Point out each Plasmodium parasite.
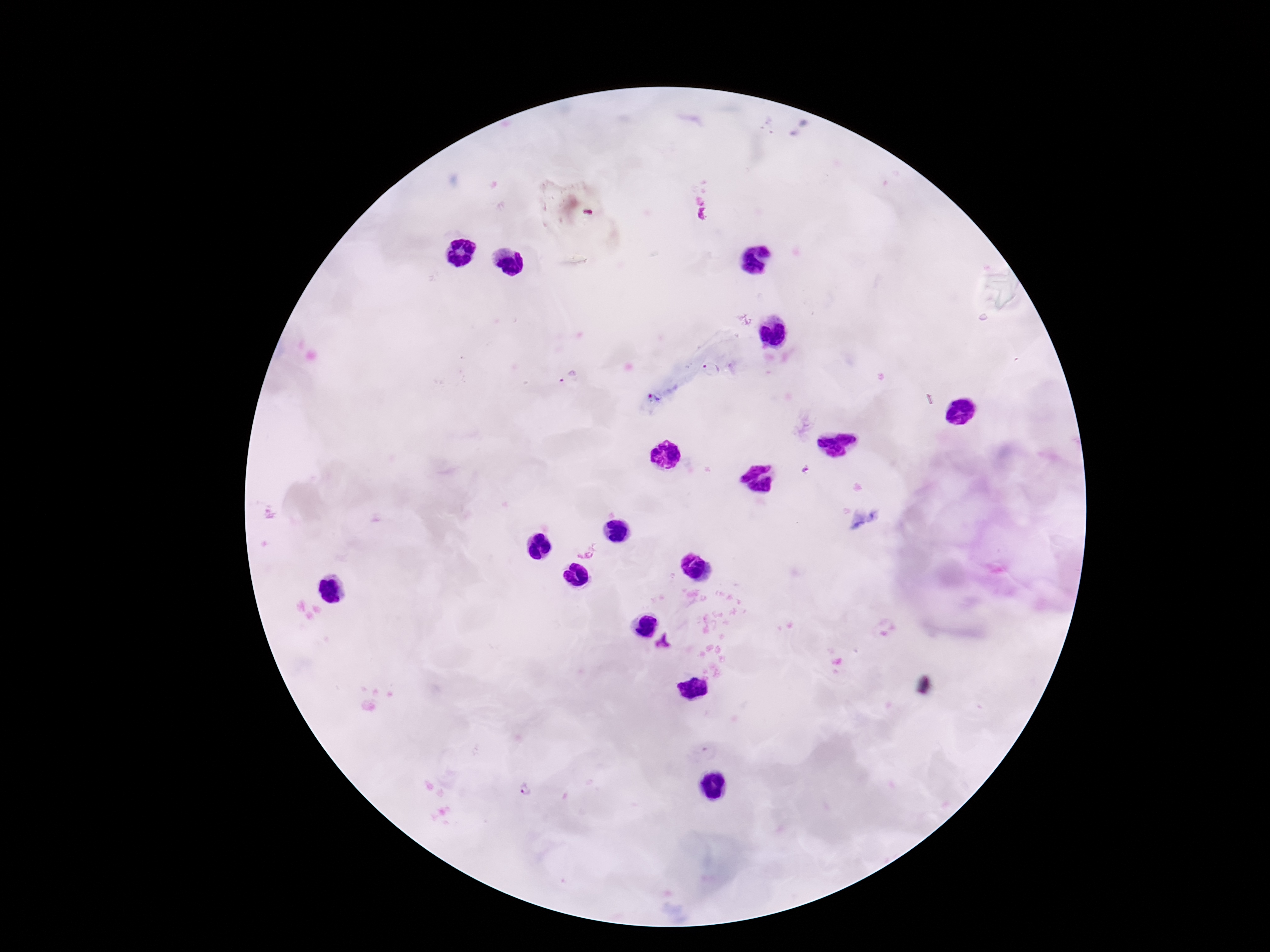
Approximate centers as {x, y} in pixels.
Plasmodium parasites: {712, 369}, {568, 378}, {584, 549}, {664, 642}, {711, 751}, {525, 790}.

Summary:
  - Image size: 1270×952 pixels
  - Preparation: thick blood film
  - Patient malaria status: infected
  - Capture: smartphone camera through the microscope eyepiece
  - Field of view: one from this slide
  - Stain: Giemsa
  - Magnification: 100x